Name the blood parasite species.
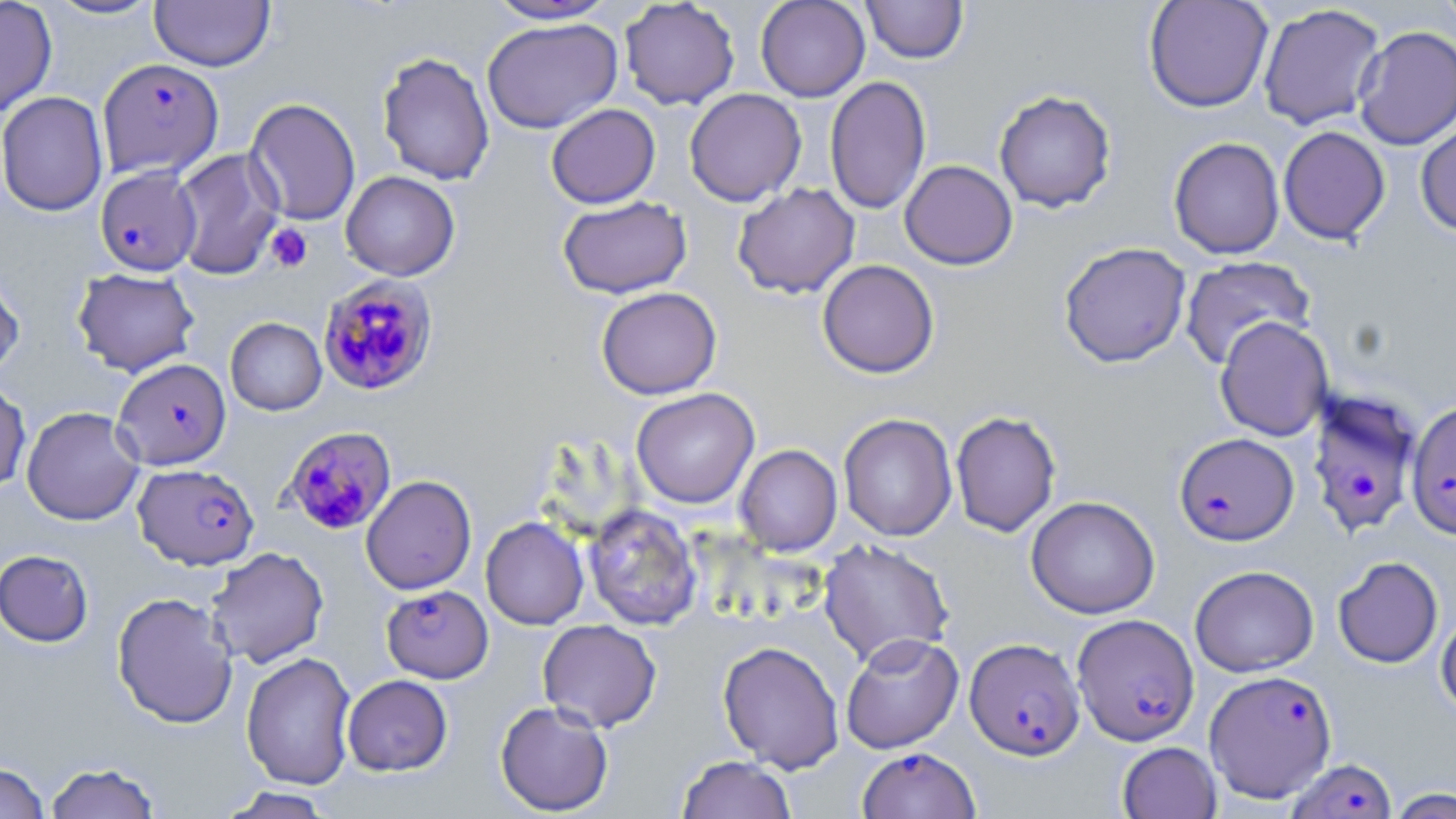
Plasmodium falciparum.

{
  "preparation": "thin blood film",
  "uninfected_red_blood_cell_locations": "approximate bounding boxes as named x1/y1/x2/y2 corners in pixels: (x1=0, y1=0, x2=57, y2=119), (x1=44, y1=0, x2=164, y2=21), (x1=619, y1=0, x2=740, y2=110), (x1=755, y1=0, x2=870, y2=101), (x1=861, y1=0, x2=968, y2=64), (x1=1143, y1=0, x2=1273, y2=113), (x1=1434, y1=0, x2=1456, y2=40), (x1=150, y1=1, x2=275, y2=71), (x1=484, y1=1, x2=620, y2=24), (x1=1257, y1=3, x2=1386, y2=130), (x1=482, y1=17, x2=622, y2=134), (x1=1353, y1=26, x2=1456, y2=151), (x1=377, y1=51, x2=495, y2=186), (x1=825, y1=75, x2=931, y2=215), (x1=684, y1=88, x2=807, y2=207), (x1=994, y1=89, x2=1116, y2=213), (x1=0, y1=91, x2=108, y2=216), (x1=244, y1=98, x2=361, y2=226), (x1=546, y1=103, x2=661, y2=209), (x1=1415, y1=117, x2=1456, y2=236), (x1=1278, y1=126, x2=1390, y2=245), (x1=1168, y1=136, x2=1285, y2=259), (x1=171, y1=148, x2=284, y2=279), (x1=899, y1=160, x2=1018, y2=270), (x1=340, y1=171, x2=460, y2=280), (x1=732, y1=183, x2=860, y2=299), (x1=558, y1=196, x2=692, y2=299), (x1=1058, y1=242, x2=1191, y2=368), (x1=1179, y1=256, x2=1316, y2=371), (x1=817, y1=260, x2=939, y2=378), (x1=0, y1=264, x2=25, y2=381), (x1=72, y1=267, x2=200, y2=376), (x1=596, y1=286, x2=722, y2=399), (x1=225, y1=317, x2=326, y2=415), (x1=1215, y1=317, x2=1334, y2=441), (x1=0, y1=377, x2=31, y2=493), (x1=631, y1=387, x2=759, y2=509), (x1=21, y1=406, x2=145, y2=525), (x1=950, y1=410, x2=1061, y2=538), (x1=838, y1=413, x2=958, y2=541), (x1=734, y1=444, x2=842, y2=556), (x1=361, y1=475, x2=476, y2=595), (x1=1026, y1=495, x2=1160, y2=619), (x1=584, y1=504, x2=702, y2=631), (x1=481, y1=517, x2=589, y2=630), (x1=818, y1=538, x2=955, y2=667), (x1=205, y1=546, x2=329, y2=669), (x1=0, y1=549, x2=94, y2=647), (x1=1332, y1=556, x2=1443, y2=669), (x1=1189, y1=565, x2=1318, y2=677), (x1=112, y1=591, x2=238, y2=729), (x1=1436, y1=609, x2=1456, y2=719), (x1=538, y1=619, x2=662, y2=732), (x1=841, y1=633, x2=964, y2=754), (x1=718, y1=640, x2=845, y2=773), (x1=241, y1=651, x2=357, y2=790), (x1=342, y1=674, x2=453, y2=776), (x1=495, y1=700, x2=614, y2=816), (x1=1117, y1=741, x2=1222, y2=819), (x1=676, y1=755, x2=796, y2=818), (x1=44, y1=761, x2=162, y2=819), (x1=0, y1=762, x2=50, y2=819), (x1=216, y1=787, x2=336, y2=818), (x1=1385, y1=788, x2=1455, y2=818)",
  "magnification": "1000x",
  "image_size": "1456×819 pixels",
  "stain": "May-Grünwald-Giemsa",
  "modality": "light microscopy",
  "field_of_view": "single",
  "plasmodium_falciparum_infected_red_blood_cell_locations": "approximate bounding boxes as named x1/y1/x2/y2 corners in pixels: (x1=97, y1=58, x2=223, y2=179), (x1=95, y1=166, x2=202, y2=276), (x1=317, y1=275, x2=438, y2=395), (x1=113, y1=358, x2=231, y2=470), (x1=1305, y1=387, x2=1423, y2=538), (x1=1406, y1=399, x2=1456, y2=540), (x1=283, y1=427, x2=396, y2=534), (x1=1174, y1=432, x2=1298, y2=546), (x1=132, y1=463, x2=259, y2=570), (x1=381, y1=585, x2=493, y2=683), (x1=1071, y1=614, x2=1199, y2=745), (x1=965, y1=637, x2=1084, y2=759), (x1=1204, y1=669, x2=1337, y2=802), (x1=857, y1=746, x2=980, y2=819), (x1=1287, y1=757, x2=1397, y2=819)",
  "platelet_locations": "approximate bounding boxes as named x1/y1/x2/y2 corners in pixels: (x1=265, y1=222, x2=313, y2=273)"
}